Locate platelets.
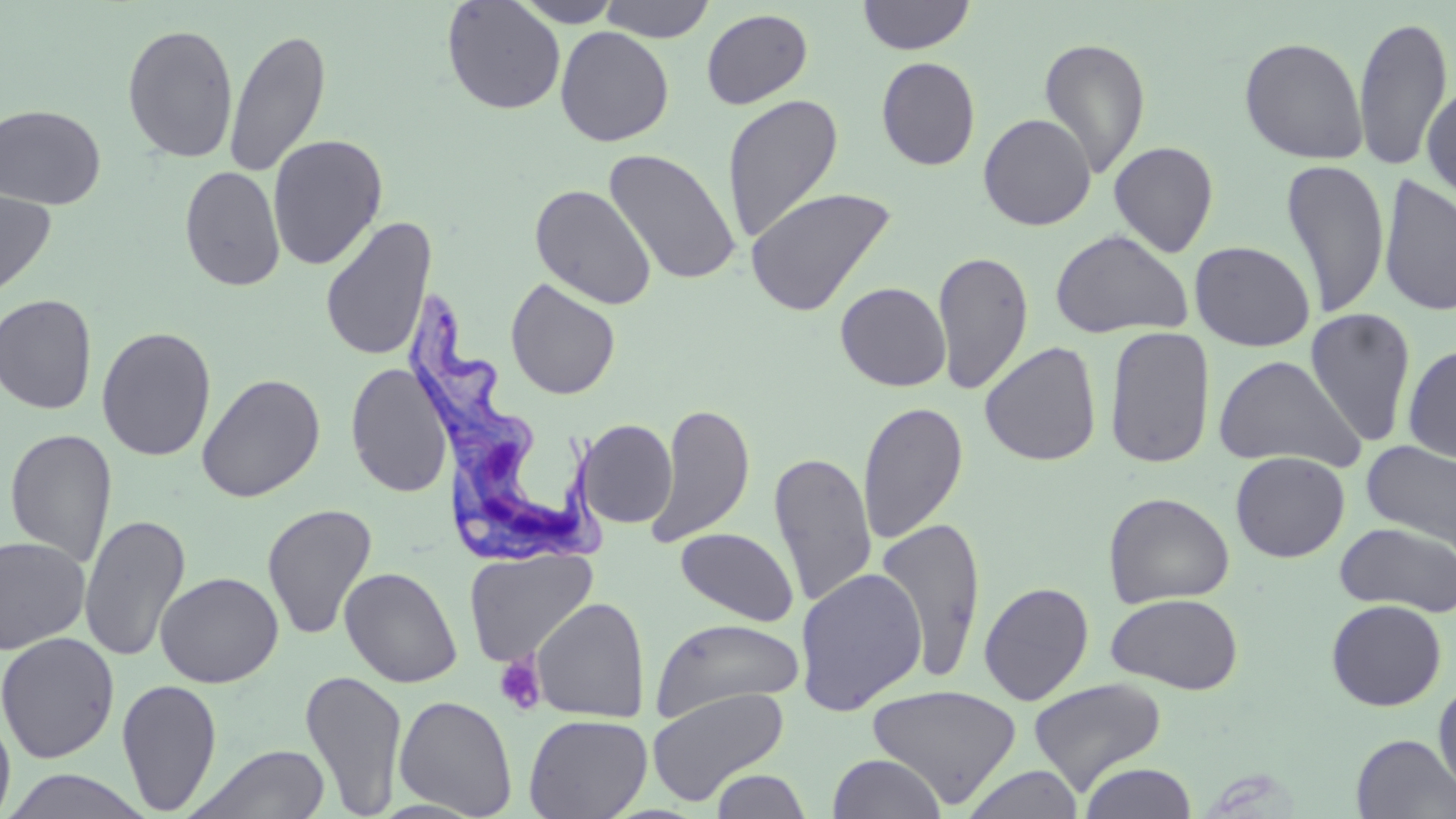
Approximate bounding boxes as (x1,y1)-(x2,y2) corner pairs in pixels.
Platelets: (494,654)-(546,715).

{
  "trypanosoma_brucei_locations": "approximate bounding boxes as (x1,y1)-(x2,y2) corner pairs in pixels: (404,290)-(610,566)",
  "slide_level_diagnosis": "Trypanosoma brucei",
  "modality": "light microscopy",
  "stain": "May-Grünwald-Giemsa",
  "preparation": "thin blood film",
  "image_size": "1456×819 pixels",
  "field_of_view": "single",
  "uninfected_red_blood_cell_locations": "approximate bounding boxes as (x1,y1)-(x2,y2) corner pairs in pixels: (512,0)-(624,27), (599,0)-(715,43), (857,0)-(976,55), (441,1)-(566,115), (701,8)-(813,109), (1353,13)-(1455,170), (122,23)-(239,163), (555,26)-(674,147), (223,27)-(332,179), (1239,36)-(1368,164), (1039,37)-(1151,179), (876,56)-(981,171), (1421,80)-(1456,203), (722,93)-(843,244), (0,104)-(107,210), (978,113)-(1096,231), (267,133)-(388,270), (1108,141)-(1219,257), (603,148)-(740,287), (1281,158)-(1390,317), (179,165)-(285,292), (1378,174)-(1456,318), (529,184)-(657,309), (745,186)-(895,317), (0,187)-(57,300), (320,214)-(437,363), (1050,229)-(1194,340), (1189,240)-(1316,352), (933,250)-(1034,396), (505,278)-(621,400), (835,281)-(951,392), (0,294)-(98,414), (1304,309)-(1417,448), (1104,325)-(1216,469), (96,326)-(217,461), (980,341)-(1102,467), (1402,343)-(1456,465), (1212,355)-(1366,471), (345,362)-(454,498), (196,373)-(326,503), (858,400)-(968,543), (649,402)-(754,548), (576,419)-(677,529), (4,427)-(118,569), (1361,440)-(1456,554), (769,450)-(877,607), (1230,451)-(1350,562), (1103,491)-(1235,608), (262,503)-(378,641), (79,514)-(191,663), (876,516)-(988,682), (1335,522)-(1456,616), (675,527)-(799,627), (0,536)-(91,654), (464,548)-(598,667), (339,566)-(462,688), (794,568)-(928,715), (155,572)-(284,688), (978,581)-(1094,705), (1105,592)-(1244,694), (532,597)-(650,722), (1326,599)-(1447,711), (651,617)-(804,721), (0,632)-(120,764), (299,669)-(408,817), (116,677)-(223,815), (1029,678)-(1167,796), (1433,678)-(1456,798), (867,684)-(1022,808), (646,688)-(790,805), (394,694)-(518,817), (0,709)-(16,819), (524,713)-(652,819), (1351,734)-(1456,818), (186,743)-(332,819), (828,753)-(946,819), (1079,761)-(1198,819), (964,765)-(1084,819), (1,769)-(153,818), (711,769)-(812,818)",
  "magnification": "1000x"
}